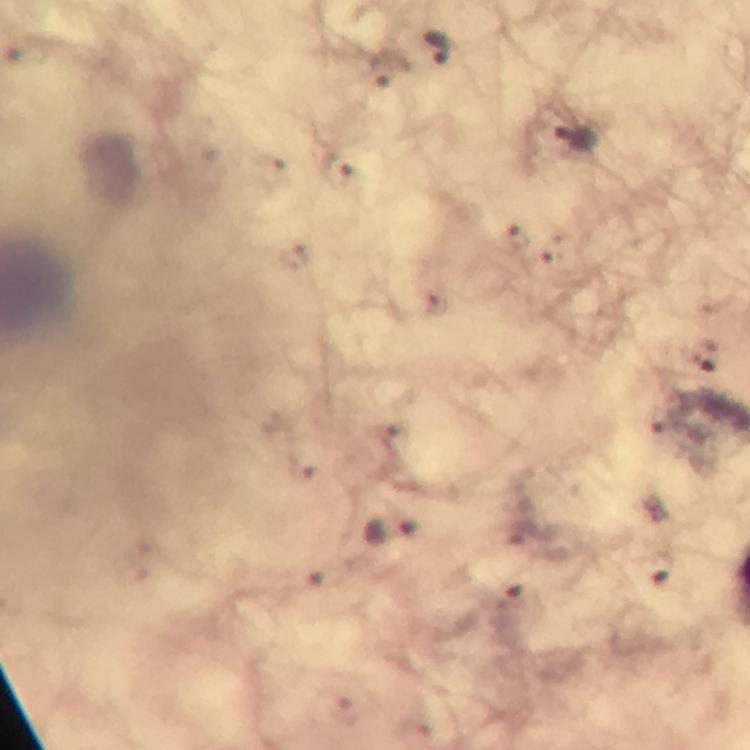

Approximate centers as [x, y] in pixels.
Summary:
  - Plasmodium parasite locations: [436, 50], [576, 137], [393, 529]
  - Immersion oil: used
  - Image size: 750×750 pixels
  - Magnification: 100x
  - Preparation: thick blood film
  - Context: from a malaria diagnostic workup
  - Cropped from: one field of view
  - Stain: Giemsa
  - Capture: smartphone mounted on the microscope